Describe the morphology of the erythrocytes.
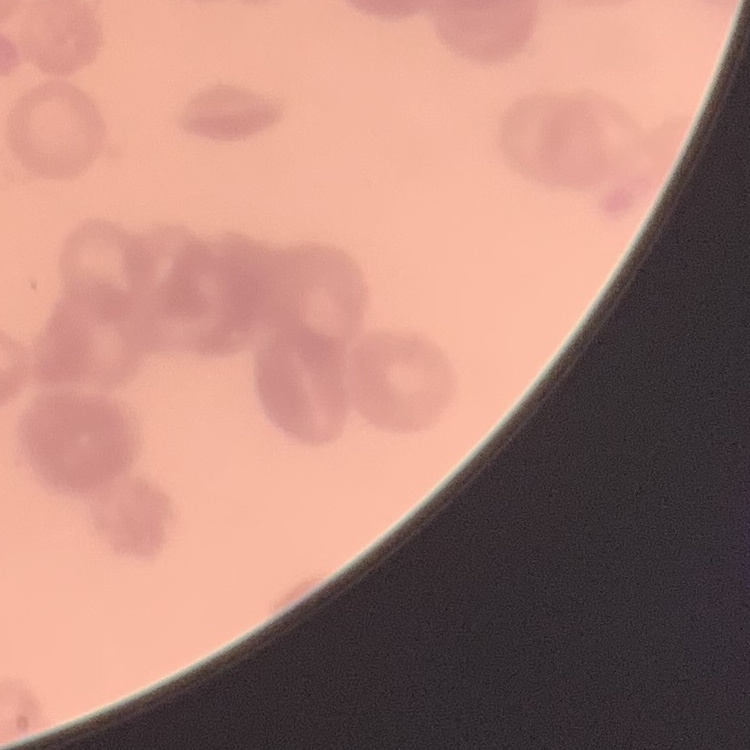

Rouleaux formation.

Summary:
  - Image type: one tile cut from a larger photomicrograph
  - Stain: Field's or Giemsa
  - Preparation: thin blood film